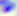
Summary:
  - Identification: Toxoplasma gondii
  - Modality: micrograph
  - Magnification: 400x